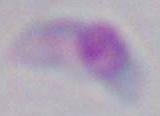
modality = micrograph
identification = Toxoplasma gondii
magnification = 1000x